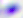

Captured at 400x magnification. Toxoplasma gondii is shown. Micrograph.